State the blood parasite species.
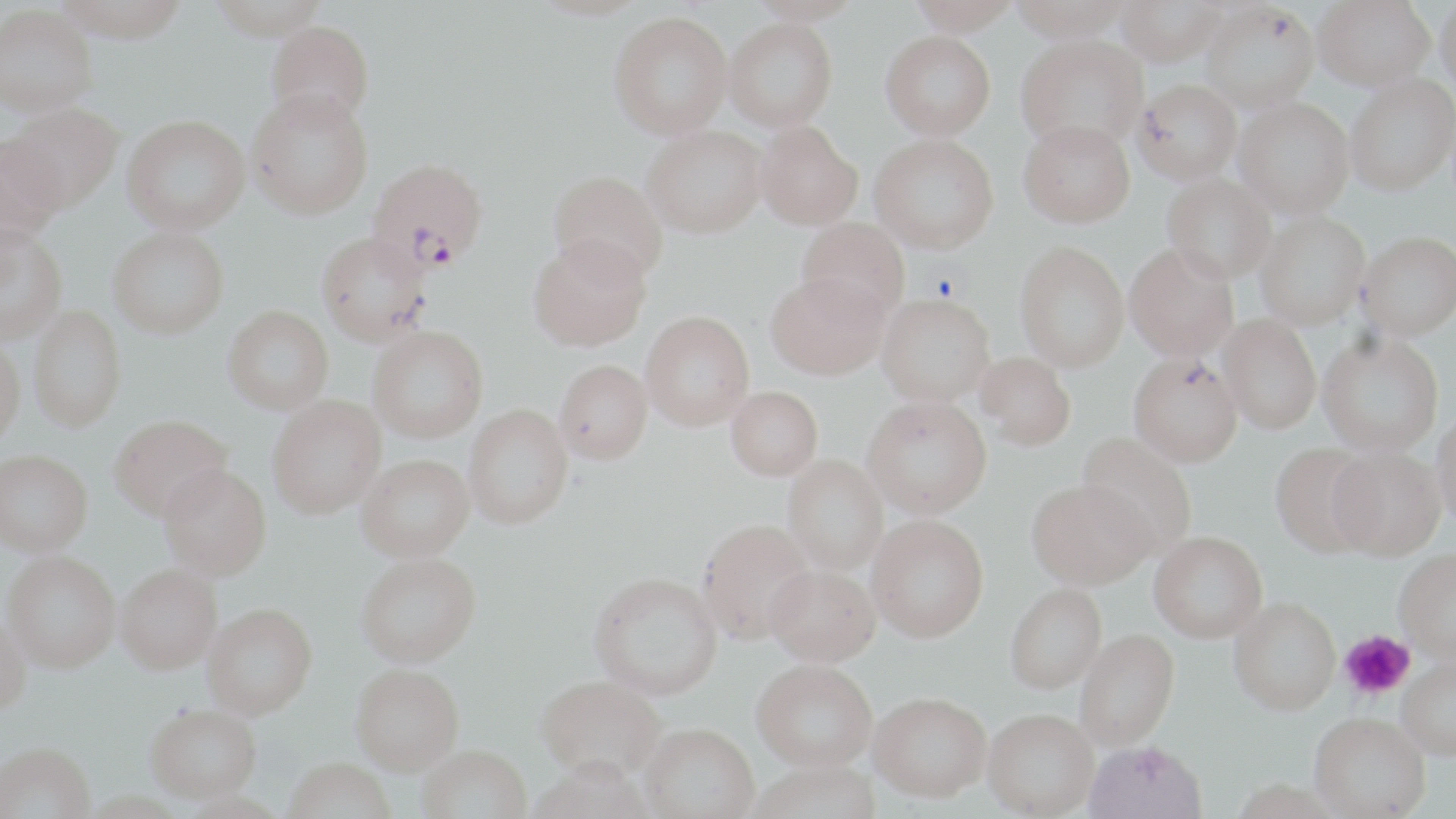

Plasmodium falciparum.

Approximate bounding boxes as [x1, y1, x2, y2] in pixels. Platelet locations: [930, 271, 959, 300], [1340, 630, 1414, 700]. Uninfected red blood cell locations: [54, 0, 193, 41], [746, 0, 865, 24], [906, 0, 1023, 35], [1009, 0, 1133, 41], [1313, 0, 1435, 91], [1435, 0, 1456, 98], [1114, 1, 1227, 66], [1201, 1, 1319, 114], [0, 4, 98, 116], [609, 11, 732, 139], [724, 18, 838, 131], [266, 20, 375, 128], [881, 31, 996, 139], [1016, 34, 1148, 152], [1345, 73, 1455, 196], [1133, 78, 1242, 184], [246, 88, 373, 220], [1234, 98, 1353, 218], [2, 103, 124, 212], [121, 114, 250, 235], [1019, 118, 1135, 228], [755, 120, 863, 230], [642, 125, 767, 238], [869, 134, 999, 253], [0, 135, 66, 245], [548, 169, 668, 283], [1163, 173, 1276, 283], [1255, 211, 1370, 330], [796, 217, 910, 321], [0, 224, 67, 344], [108, 227, 229, 338], [1358, 231, 1456, 340], [316, 232, 431, 346], [528, 237, 651, 352], [1015, 241, 1130, 372], [1124, 243, 1239, 361], [766, 272, 890, 380], [877, 293, 995, 406], [28, 305, 127, 431], [223, 305, 334, 414], [641, 311, 755, 430], [1218, 314, 1321, 434], [368, 325, 488, 442], [1317, 332, 1443, 456], [0, 337, 26, 446], [976, 352, 1076, 450], [1129, 352, 1243, 467], [555, 359, 652, 464], [726, 386, 823, 480], [862, 395, 991, 518], [267, 396, 386, 518], [464, 404, 573, 529], [1432, 409, 1456, 530], [108, 413, 232, 521], [1077, 433, 1198, 555], [1270, 442, 1378, 558], [1328, 445, 1446, 560], [1, 450, 93, 555], [358, 454, 474, 560], [783, 455, 888, 574], [158, 464, 272, 581], [1027, 479, 1155, 589], [867, 514, 989, 642], [697, 518, 816, 644], [1149, 531, 1268, 643], [1394, 548, 1456, 662], [2, 550, 121, 672], [357, 552, 481, 667], [115, 563, 222, 674], [765, 564, 879, 665], [589, 572, 722, 699], [1005, 583, 1107, 693], [1229, 597, 1341, 715], [202, 604, 317, 718], [0, 613, 31, 714], [1075, 629, 1180, 750], [1397, 657, 1456, 760], [752, 659, 876, 770], [351, 663, 464, 773], [536, 674, 667, 782], [870, 691, 992, 801], [145, 704, 261, 802], [982, 708, 1098, 817], [1309, 712, 1430, 818], [640, 723, 760, 819], [1084, 739, 1208, 819], [1, 741, 95, 819], [418, 745, 532, 819], [284, 757, 396, 819], [748, 761, 881, 819]. Plasmodium falciparum-infected red blood cell locations: [366, 157, 488, 273]. 1000x magnification. One field of a larger specimen. May-Grünwald-Giemsa stain. Thin blood smear. Image is 1456×819 pixels. Light microscopy.